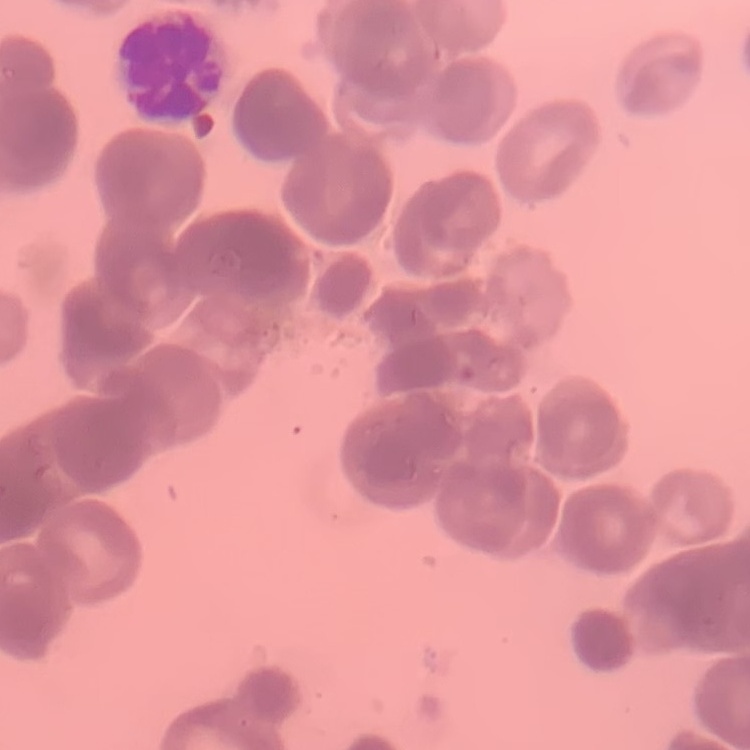

The erythrocytes show rouleaux formation. Thin blood film. Field's or Giemsa stain. Square crop of a larger photomicrograph.